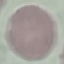
Result: no malaria parasites detected. Photographed with a smartphone camera at the microscope eyepiece. Thin smear of blood. Cell patch, automatically extracted from a larger field of view and resized to 64 × 64 pixels. Giemsa-stained preparation.